Locate every Plasmodium falciparum parasite and give its life-cycle stage, and locate every leukocyte and any debris.
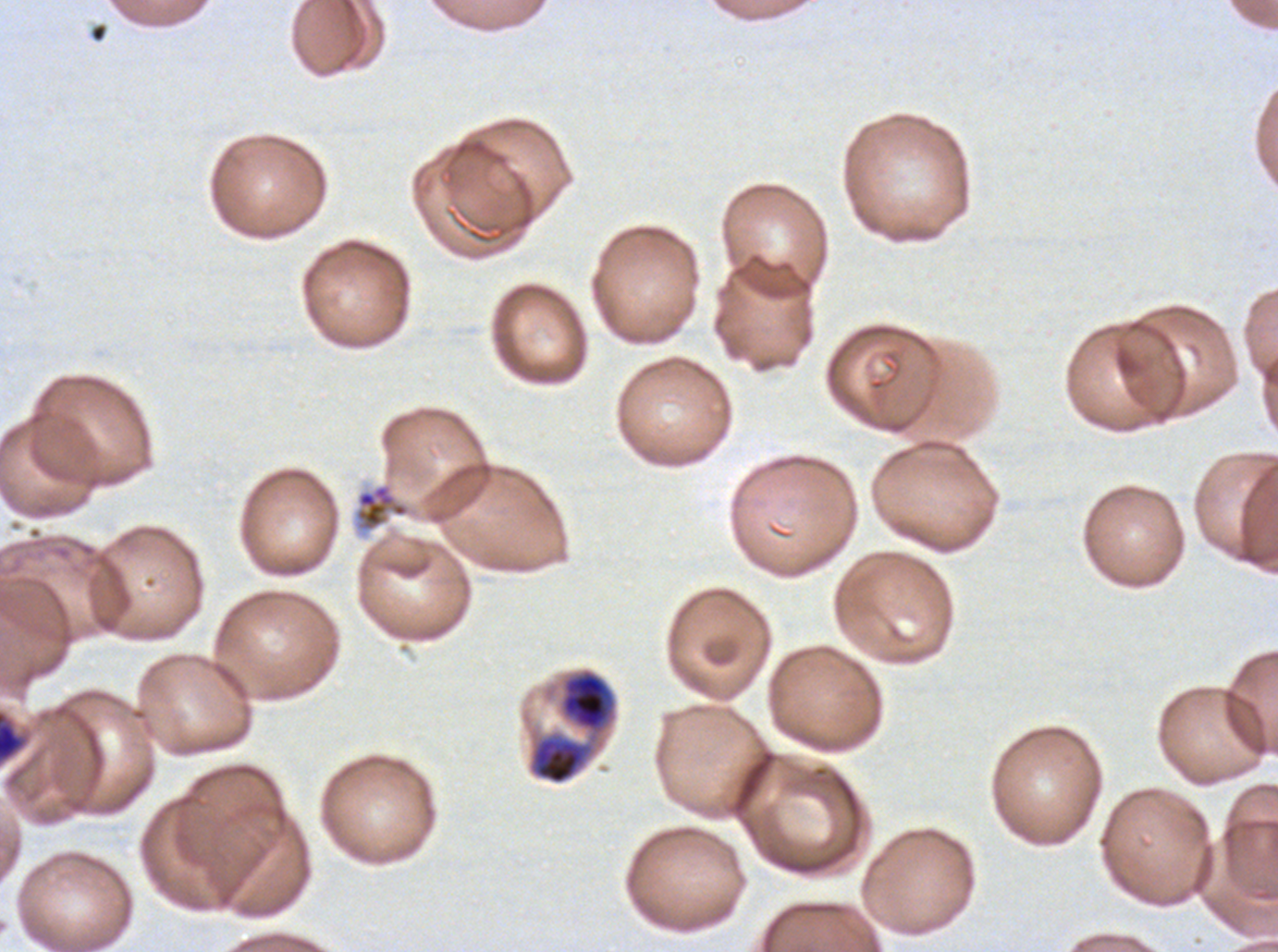

Approximate bounding boxes as {x1, y1, x2, y2} in pixels.
Late trophozoites: {559, 669, 616, 733}.
Early schizonts: {530, 735, 593, 785}.
Segmenters: {353, 482, 411, 532}.
Debris: {90, 23, 107, 43}, {0, 711, 25, 763}.
No rings, late-ring/early-trophozoite forms, mid trophozoites, late schizonts, gametocytes, or leukocytes observed.

preparation: thin blood smear
field_of_view: one sub-image of a larger composite
specimen: Plasmodium falciparum cultured ex vivo for 24 to 48 hours, from a patient in The Gambia
image_size: 1278×952 pixels
stain: Giemsa
life_cycle_stages_observed: late trophozoite, early schizont, segmenter